Classify this cell by malaria status.
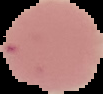

It is uninfected.

From a thin blood film. Cell region segmented out of the field of view; the surrounding area is masked to black. Image is 103×94 pixels.